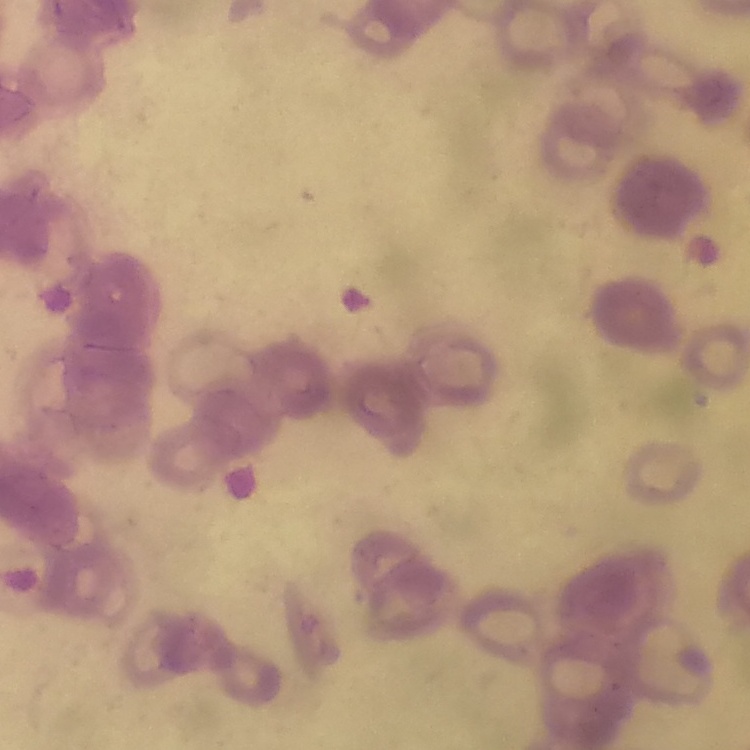

The erythrocytes exhibit rouleaux formation. Stained with either Field's or Giemsa. Thin blood smear. Square crop of a larger photomicrograph.